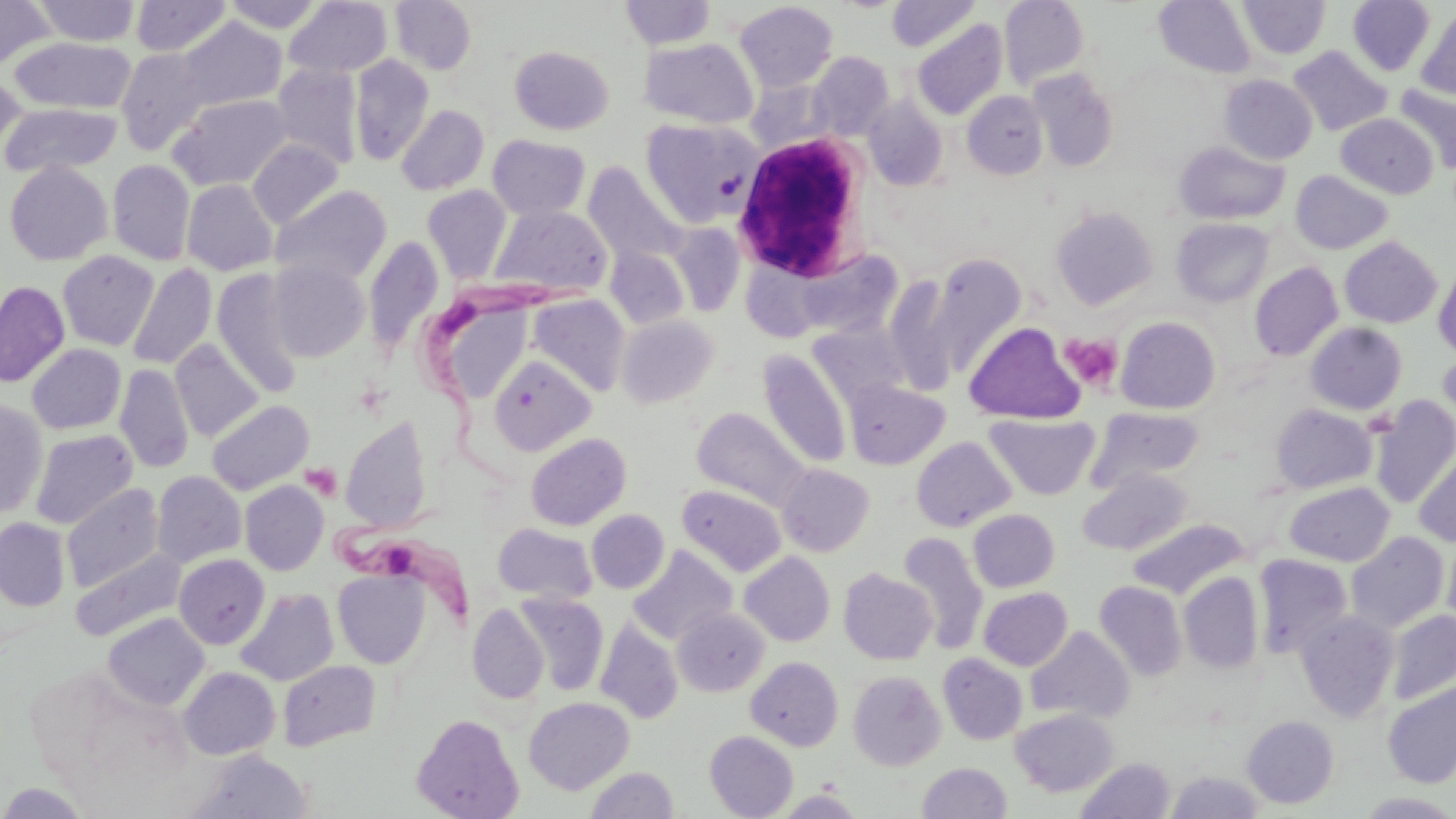

slide-level diagnosis = Trypanosoma brucei
preparation = thin blood smear
magnification = 1000x
image size = 1456×819 pixels
modality = optical microscopy
white blood cell locations = approximate bounding boxes as (x1,y1)-(x2,y2) corner pairs in pixels: (730,128)-(876,286)
uninfected red blood cell locations = approximate bounding boxes as (x1,y1)-(x2,y2) corner pairs in pixels: (0,0)-(56,70), (130,0)-(232,57), (222,0)-(326,32), (390,0)-(477,74), (620,0)-(716,50), (887,0)-(980,51), (1000,0)-(1089,89), (1154,0)-(1257,78), (1238,0)-(1331,59), (1348,0)-(1435,75), (35,1)-(140,46), (285,1)-(392,79), (734,2)-(838,92), (1415,7)-(1456,99), (175,17)-(286,111), (912,18)-(1008,120), (641,37)-(759,128), (10,38)-(136,114), (509,45)-(614,135), (1288,45)-(1392,136), (116,48)-(214,155), (807,51)-(894,140), (349,55)-(434,165), (272,64)-(363,170), (1027,69)-(1120,172), (0,70)-(27,161), (1219,74)-(1317,165), (1395,85)-(1456,174), (962,91)-(1049,179), (168,93)-(292,191), (863,95)-(948,191), (1,102)-(122,179), (396,104)-(489,195), (1336,114)-(1438,199), (641,117)-(761,226), (487,135)-(590,220), (248,138)-(344,228), (1174,140)-(1290,225), (108,160)-(195,266), (4,161)-(112,265), (584,162)-(685,267), (1290,170)-(1393,254), (182,180)-(278,276), (270,185)-(392,287), (422,185)-(512,283), (489,204)-(612,298), (504,204)-(620,394), (1050,206)-(1158,310), (1172,218)-(1273,307), (666,221)-(746,316), (364,234)-(445,355), (1339,236)-(1442,328), (606,247)-(691,330), (788,248)-(909,342), (57,250)-(159,351), (928,253)-(1028,375), (267,258)-(370,361), (1433,260)-(1456,362), (1250,262)-(1343,361), (128,263)-(217,371), (212,270)-(304,396), (883,274)-(959,394), (0,280)-(70,387), (529,294)-(631,396), (618,315)-(720,407), (1116,316)-(1221,414), (965,322)-(1085,424), (1305,322)-(1407,414), (809,324)-(911,408), (171,340)-(264,442), (27,344)-(126,434), (757,350)-(852,470), (1438,350)-(1456,439), (489,354)-(596,456), (115,364)-(194,473), (843,380)-(950,469), (1370,396)-(1456,508), (0,400)-(48,518), (207,400)-(313,495), (1270,404)-(1377,493), (692,406)-(810,511), (1088,406)-(1204,491), (985,413)-(1101,500), (341,417)-(432,532), (30,429)-(138,529), (526,433)-(631,530), (912,436)-(1015,532), (1414,451)-(1456,547), (777,463)-(875,556), (1077,468)-(1192,555), (152,470)-(246,568), (240,481)-(329,575), (1284,481)-(1395,566), (62,483)-(164,594), (677,484)-(787,577), (968,509)-(1059,592), (586,510)-(669,593), (1,518)-(70,610), (1128,519)-(1247,598), (493,523)-(597,604), (1347,532)-(1449,632), (897,533)-(989,655), (1443,535)-(1456,635), (629,546)-(736,645), (72,550)-(185,642), (740,552)-(835,647), (174,554)-(269,649), (1253,554)-(1352,659), (333,569)-(430,669), (839,569)-(937,664), (1179,572)-(1264,673), (1094,581)-(1187,680), (979,587)-(1072,670), (236,588)-(339,686), (514,592)-(609,695), (468,603)-(549,704), (673,606)-(770,697), (1387,609)-(1455,704), (1296,610)-(1399,722), (104,613)-(210,710), (596,620)-(683,723), (1026,626)-(1134,724), (938,653)-(1028,745), (746,657)-(843,751), (277,660)-(381,751), (179,666)-(280,759), (848,671)-(946,770), (1383,681)-(1456,787), (523,696)-(634,795), (1011,708)-(1118,796), (412,714)-(524,819), (1242,715)-(1339,808), (705,730)-(798,818), (187,749)-(313,818), (1075,757)-(1175,819), (918,762)-(1013,819), (586,767)-(678,819), (1166,771)-(1264,818)
stain = May-Grünwald-Giemsa
platelet locations = approximate bounding boxes as (x1,y1)-(x2,y2) corner pairs in pixels: (717,171)-(748,200), (1059,332)-(1123,392), (301,463)-(343,500)
Trypanosoma brucei locations = approximate bounding boxes as (x1,y1)-(x2,y2) corner pairs in pixels: (412,271)-(563,491), (330,498)-(480,624)
field of view = single